Give the extent of all Trypanosoma brucei.
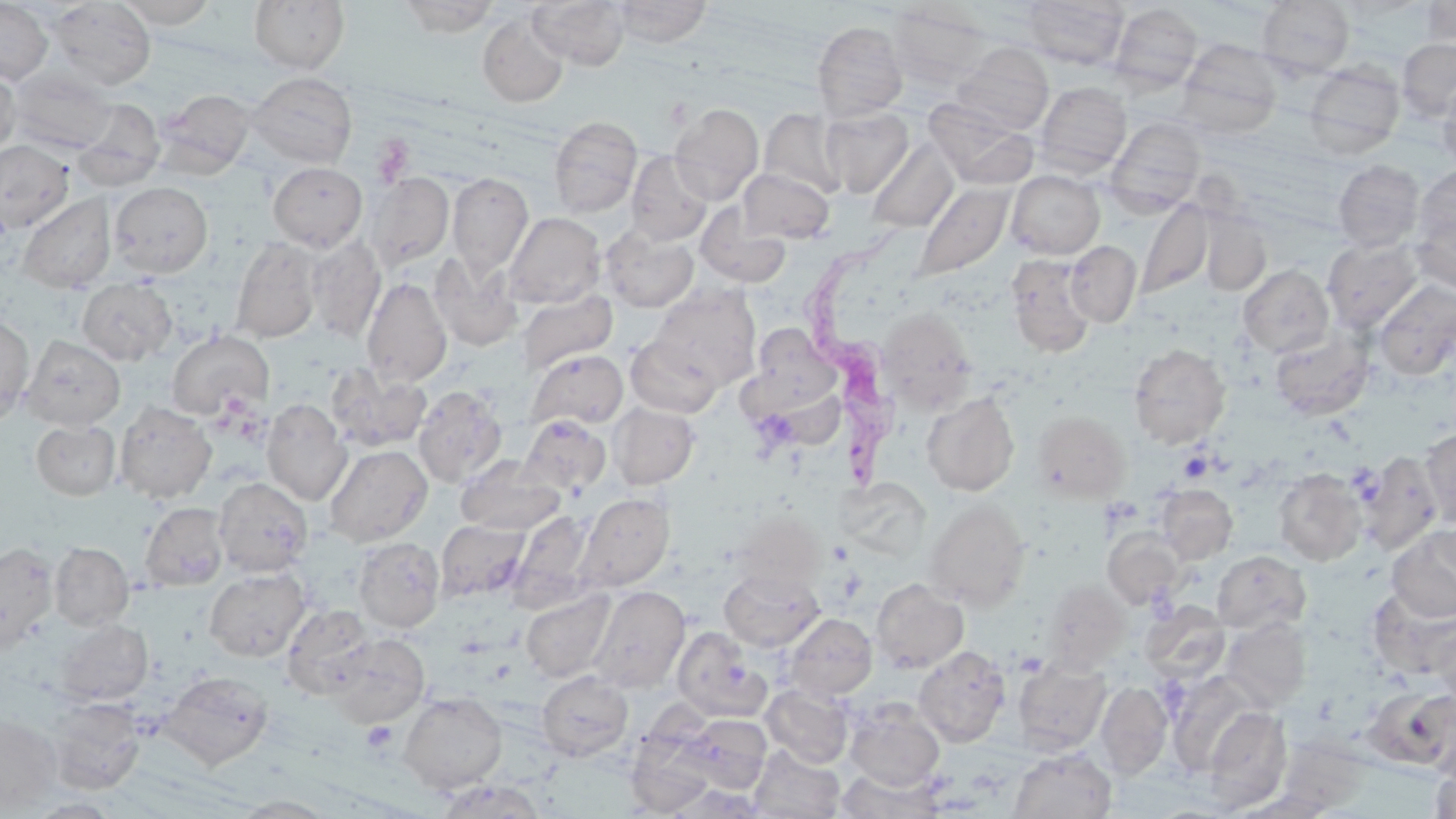

Approximate bounding boxes as [x1, y1, x2, y2] in pixels.
Trypanosoma brucei: [799, 227, 916, 498].

slide-level diagnosis = Trypanosoma brucei
field of view = single
preparation = thin blood smear
modality = optical microscopy
stain = May-Grünwald-Giemsa
magnification = 1000x
platelet locations = approximate bounding boxes as [x1, y1, x2, y2] in pixels: [369, 134, 415, 185], [1178, 451, 1214, 483], [361, 721, 398, 752]
image size = 1456×819 pixels
uninfected red blood cell locations = approximate bounding boxes as [x1, y1, x2, y2] in pixels: [115, 0, 218, 28], [249, 0, 349, 74], [398, 0, 500, 37], [529, 0, 629, 70], [610, 0, 712, 47], [1021, 0, 1128, 69], [0, 1, 53, 84], [48, 1, 156, 90], [1257, 1, 1355, 78], [1421, 1, 1456, 47], [1109, 3, 1203, 93], [888, 4, 991, 89], [477, 12, 569, 107], [812, 21, 907, 121], [1177, 37, 1284, 137], [1397, 38, 1456, 122], [952, 43, 1054, 134], [1304, 62, 1405, 157], [0, 64, 19, 158], [8, 67, 115, 156], [248, 71, 357, 168], [1437, 76, 1456, 174], [1035, 81, 1131, 175], [155, 87, 256, 177], [73, 98, 165, 191], [924, 99, 1037, 188], [668, 103, 764, 205], [821, 106, 914, 198], [759, 108, 846, 199], [549, 116, 643, 218], [1106, 116, 1206, 212], [866, 139, 960, 233], [0, 140, 73, 233], [625, 151, 712, 246], [1333, 160, 1425, 251], [268, 162, 367, 250], [1414, 163, 1456, 250], [738, 169, 835, 244], [1006, 170, 1104, 259], [365, 172, 454, 270], [448, 172, 533, 278], [913, 181, 1014, 281], [109, 182, 212, 278], [18, 194, 116, 292], [1137, 199, 1212, 300], [695, 202, 791, 290], [1412, 208, 1456, 293], [1200, 211, 1271, 295], [503, 212, 605, 308], [601, 227, 698, 312], [305, 236, 386, 342], [230, 237, 322, 343], [1322, 237, 1424, 334], [1065, 241, 1141, 327], [428, 251, 524, 351], [1005, 253, 1097, 357], [1238, 265, 1334, 358], [362, 277, 452, 387], [76, 278, 177, 365], [1372, 279, 1456, 380], [651, 285, 761, 391], [516, 289, 618, 374], [877, 309, 977, 413], [0, 315, 34, 424], [749, 324, 842, 411], [1269, 328, 1375, 420], [166, 330, 275, 419], [21, 335, 126, 430], [626, 336, 723, 419], [1129, 343, 1230, 449], [527, 349, 628, 430], [326, 364, 431, 453], [413, 385, 507, 487], [922, 392, 1020, 496], [261, 398, 352, 506], [115, 401, 216, 503], [610, 402, 699, 489], [1034, 410, 1130, 502], [518, 415, 611, 496], [31, 420, 120, 499], [1420, 427, 1456, 529], [324, 445, 432, 547], [1356, 453, 1443, 555], [456, 456, 565, 536], [1274, 469, 1367, 566], [214, 478, 312, 577], [835, 478, 931, 563], [1156, 484, 1238, 564], [574, 492, 674, 592], [924, 499, 1031, 611], [140, 502, 229, 591], [512, 510, 595, 606], [731, 510, 825, 593], [437, 519, 531, 601], [1388, 526, 1456, 622], [1103, 527, 1186, 608], [353, 537, 445, 632], [0, 542, 58, 652], [50, 542, 134, 630], [1212, 550, 1311, 635], [204, 567, 310, 661], [719, 567, 824, 652], [871, 579, 969, 673], [1041, 579, 1131, 673], [588, 585, 690, 693], [521, 587, 617, 683], [1368, 588, 1456, 679], [1142, 602, 1229, 683], [281, 604, 376, 698], [784, 613, 877, 701], [1221, 616, 1311, 712], [1430, 617, 1456, 706], [55, 619, 152, 706], [672, 626, 771, 722], [329, 634, 429, 727], [914, 645, 1011, 747], [1013, 659, 1111, 756], [159, 671, 272, 769], [536, 671, 633, 761], [1096, 680, 1172, 781], [761, 684, 854, 768], [1373, 686, 1456, 771], [398, 691, 507, 793], [46, 698, 146, 794], [845, 702, 945, 791], [1202, 705, 1292, 812], [0, 713, 62, 812], [677, 714, 771, 794], [1278, 717, 1373, 819], [625, 726, 718, 817], [749, 745, 845, 819], [1429, 745, 1456, 819], [1007, 748, 1116, 819], [836, 768, 943, 818], [434, 779, 547, 818], [229, 795, 339, 817]